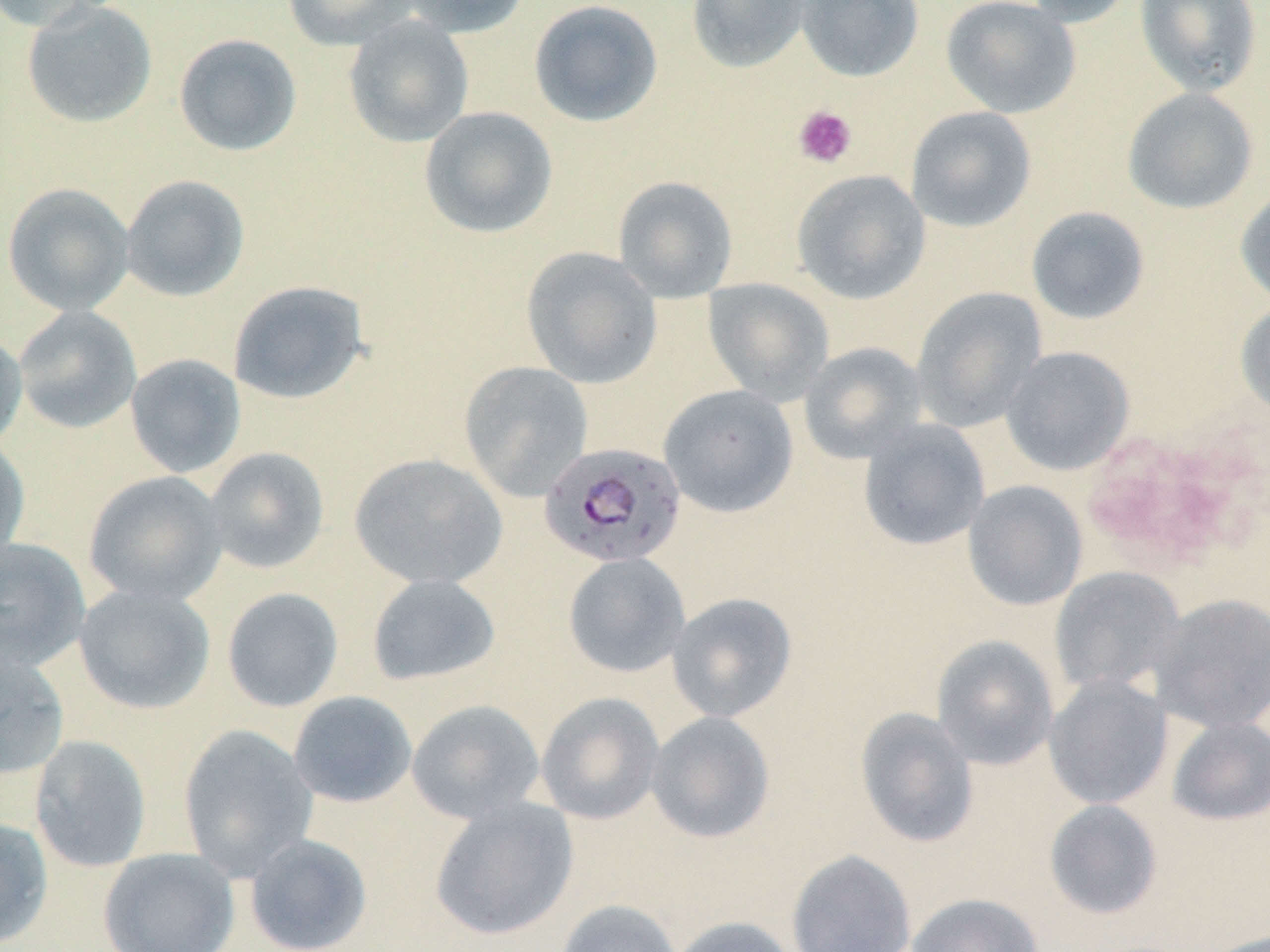
Summary:
  - Coordinate format: approximate bounding boxes as (x1, y1, x2, y2) in pixels
  - Platelet locations: (793, 104, 857, 169)
  - Uninfected red blood cell locations: (0, 0, 124, 33), (282, 0, 420, 50), (396, 0, 532, 38), (528, 0, 664, 128), (686, 0, 813, 74), (796, 0, 923, 82), (941, 0, 1081, 119), (1019, 0, 1136, 27), (1134, 0, 1262, 97), (21, 1, 158, 129), (343, 15, 474, 147), (173, 32, 302, 156), (1122, 87, 1259, 215), (419, 106, 558, 239), (905, 106, 1037, 232), (791, 169, 930, 304), (120, 174, 250, 302), (613, 176, 738, 302), (2, 182, 135, 316), (1235, 185, 1270, 308), (1026, 206, 1151, 325), (520, 246, 662, 389), (702, 277, 835, 405), (228, 279, 370, 405), (911, 287, 1048, 433), (1234, 301, 1270, 419), (12, 306, 142, 434), (0, 328, 28, 453), (798, 342, 928, 464), (1000, 346, 1135, 475), (124, 353, 246, 478), (459, 361, 593, 501), (658, 384, 799, 518), (857, 419, 990, 551), (0, 434, 31, 564), (203, 446, 330, 575), (348, 453, 508, 590), (82, 471, 228, 606), (962, 480, 1088, 611), (0, 536, 91, 670), (563, 552, 690, 678), (1050, 566, 1186, 698), (366, 574, 501, 686), (73, 583, 216, 715), (221, 587, 344, 712), (667, 592, 798, 722), (1151, 592, 1270, 734), (931, 634, 1059, 770), (0, 647, 69, 782), (1043, 674, 1173, 810), (288, 690, 417, 808), (535, 691, 665, 825), (406, 699, 545, 824), (854, 707, 979, 848), (646, 710, 776, 844), (1166, 716, 1270, 826), (177, 724, 318, 879), (29, 735, 152, 873), (428, 796, 579, 941), (1044, 799, 1163, 919), (0, 816, 53, 949), (244, 833, 373, 952), (98, 847, 240, 952), (786, 849, 917, 952), (906, 892, 1045, 952), (556, 899, 683, 952), (666, 916, 800, 952), (1200, 930, 1270, 952)
  - Plasmodium falciparum-infected red blood cell locations: (544, 439, 691, 566)
  - Slide-level diagnosis: Plasmodium falciparum
  - Modality: optical microscopy
  - Stain: May-Grünwald-Giemsa
  - Magnification: 1000x
  - Field of view: single
  - Preparation: thin blood smear
  - Image size: 1270×952 pixels